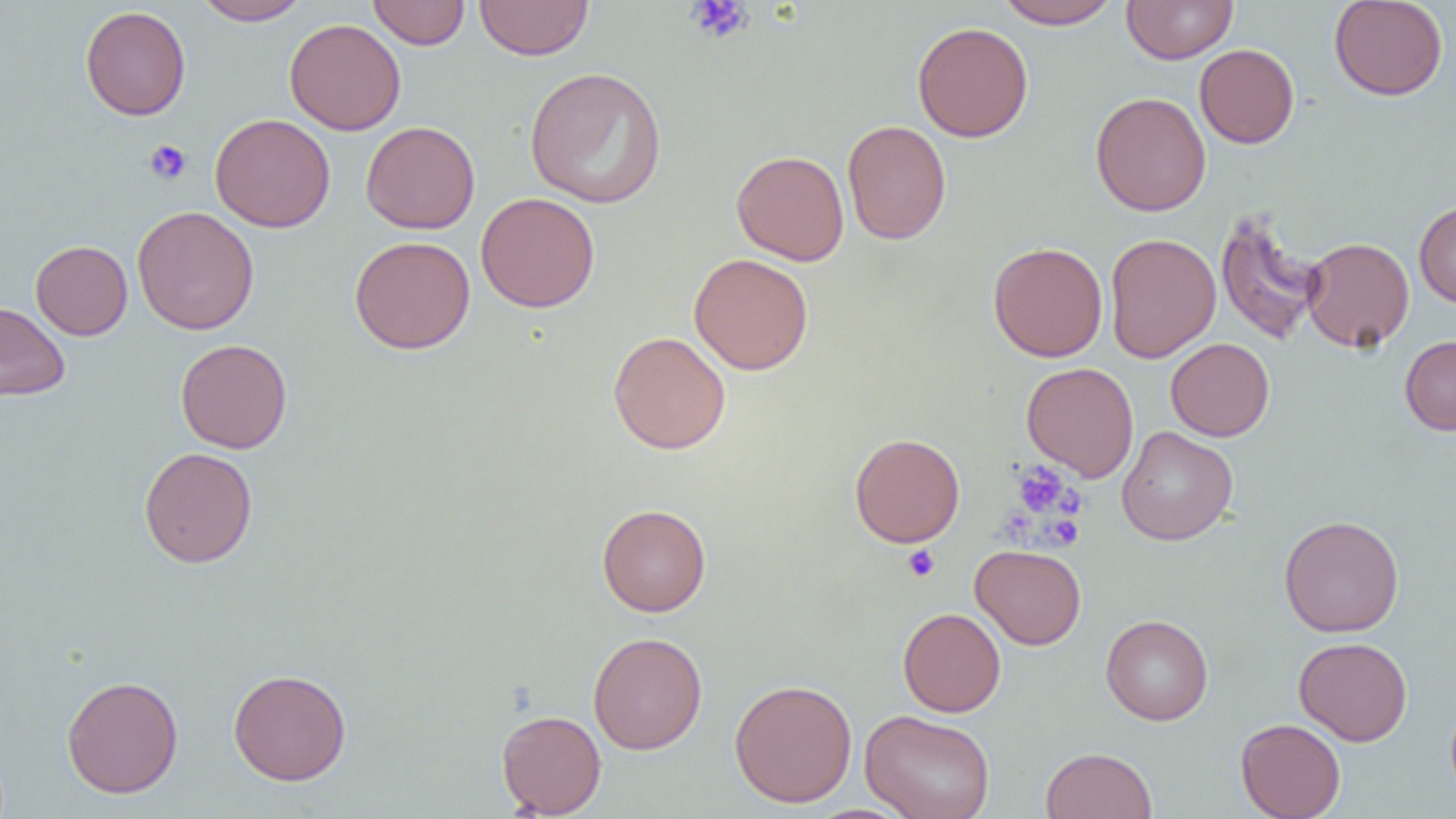
Summary:
  - Coordinate format: approximate bounding boxes as (x1, y1, x2, y2) in pixels
  - Platelet locations: (686, 0, 753, 43), (144, 139, 191, 185), (1013, 462, 1074, 518), (1046, 515, 1083, 549), (902, 544, 940, 581)
  - Uninfected red blood cell locations: (192, 0, 311, 25), (474, 0, 594, 60), (993, 0, 1122, 29), (1122, 0, 1238, 64), (1328, 0, 1448, 101), (367, 1, 470, 49), (80, 5, 191, 120), (284, 18, 406, 135), (912, 21, 1033, 142), (1194, 43, 1299, 148), (523, 66, 667, 209), (1090, 91, 1211, 216), (210, 113, 336, 232), (360, 120, 480, 234), (842, 120, 951, 245), (732, 150, 850, 266), (475, 192, 600, 313), (1414, 201, 1456, 307), (132, 206, 259, 334), (1214, 209, 1325, 345), (1104, 233, 1221, 364), (349, 236, 475, 354), (1301, 236, 1414, 352), (30, 240, 133, 340), (988, 241, 1108, 362), (689, 253, 813, 375), (0, 300, 70, 401), (607, 331, 731, 454), (1399, 335, 1456, 435), (175, 338, 292, 453), (1165, 338, 1274, 441), (1021, 362, 1139, 481), (1116, 426, 1238, 545), (849, 432, 965, 548), (139, 446, 257, 568), (597, 503, 711, 616), (1278, 515, 1404, 637), (970, 544, 1086, 650), (898, 607, 1006, 717), (1100, 614, 1214, 725), (588, 631, 707, 754), (1293, 636, 1412, 746), (228, 668, 351, 786), (61, 675, 184, 798), (729, 678, 857, 807), (1445, 694, 1456, 806), (860, 709, 995, 819), (496, 710, 606, 817), (1235, 718, 1346, 819), (1041, 747, 1158, 819)
  - Slide-level diagnosis: negative for blood parasites
  - Image size: 1456×819 pixels
  - Preparation: thin blood film
  - Modality: optical microscopy
  - Field of view: single
  - Magnification: 1000x